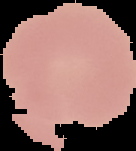 Cell region segmented out of the field of view; the surrounding area is masked to black. Image is 136×151 pixels. Malaria status: uninfected. From a thin blood smear.